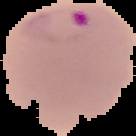

malaria status = parasitized
image size = 136×136 pixels
image type = segmented cell region with the area outside set to black
preparation = thin blood film